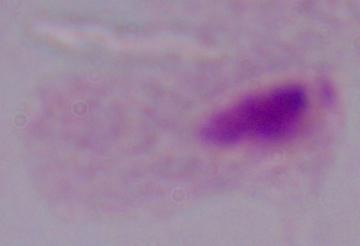
identification = trichomonad
modality = micrograph
magnification = 1000x